Identify the parasite.
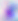

Toxoplasma gondii.

modality = micrograph
magnification = 400x